Locate Plasmodium parasites and leukocytes.
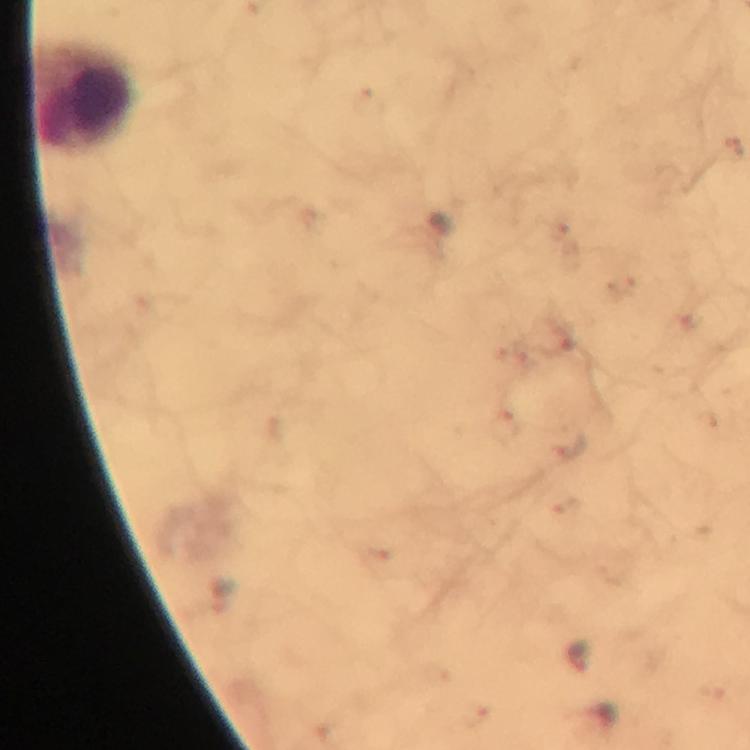

No Plasmodium parasites seen.
Approximate centers as (x, y) in pixels.
Leukocytes: (83, 97).

image_size: 750×750 pixels
preparation: thick blood film
immersion_oil: used
context: from a malaria diagnostic workup
stain: Giemsa
magnification: 100x
capture: smartphone photograph through a microscope
cropped_from: one field of view